Assess the morphology of the red blood cells.
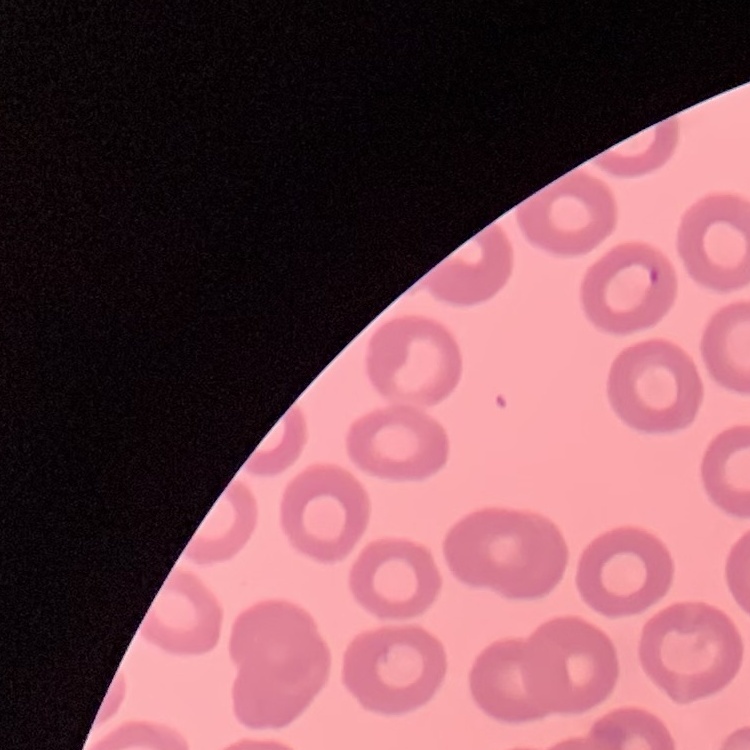

They show no rouleaux formation.

{
  "preparation": "thin blood film",
  "image_type": "one tile cut from a larger photomicrograph",
  "stain": "Field's or Giemsa"
}